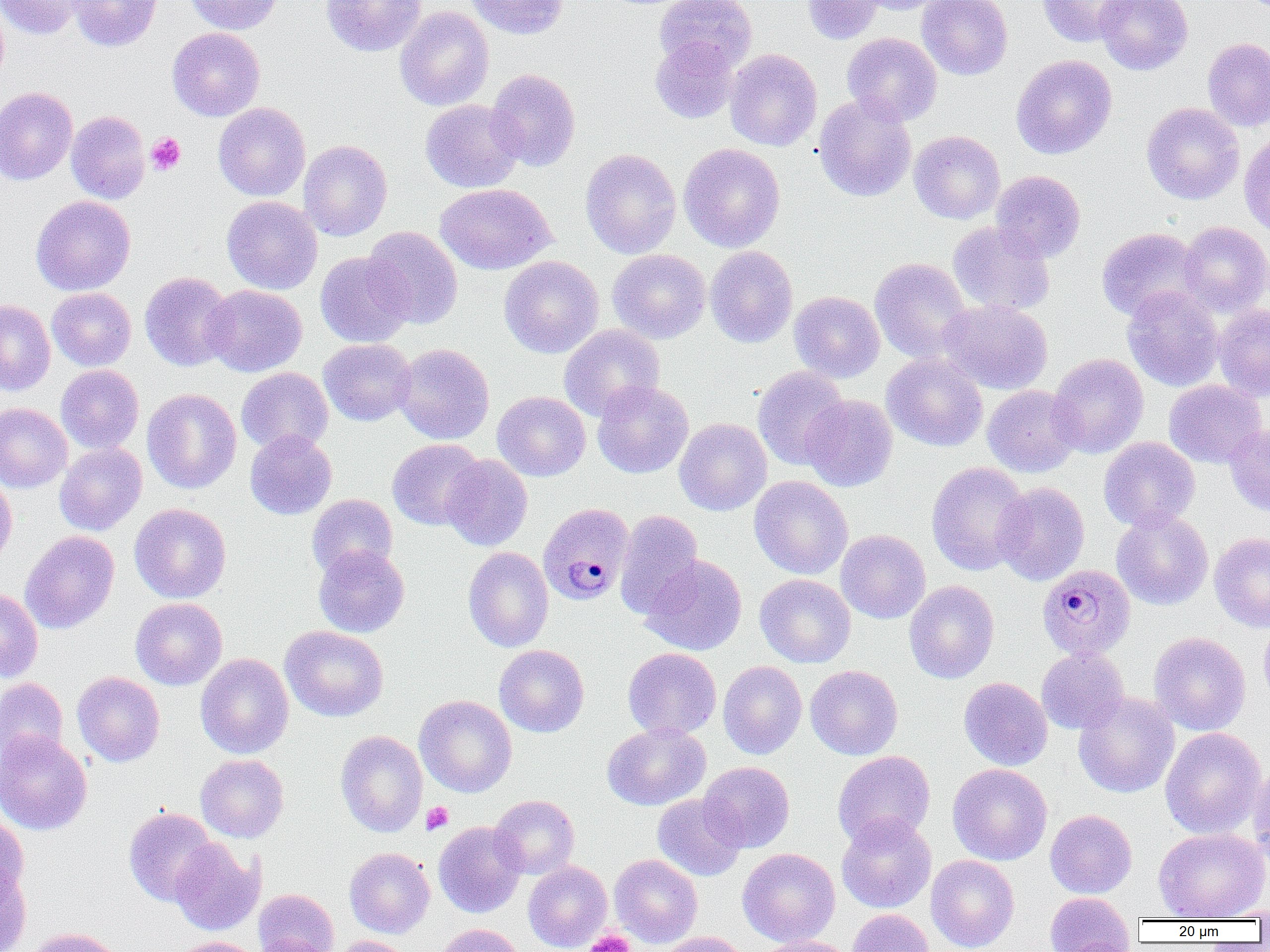

slide-level diagnosis = Plasmodium malariae
uninfected red blood cell locations = approximate bounding boxes as named x1/y1/x2/y2 corners in pixels: (x1=0, y1=0, x2=85, y2=39), (x1=66, y1=0, x2=162, y2=52), (x1=184, y1=0, x2=283, y2=34), (x1=321, y1=0, x2=426, y2=56), (x1=464, y1=0, x2=570, y2=39), (x1=655, y1=0, x2=757, y2=73), (x1=801, y1=0, x2=885, y2=44), (x1=857, y1=0, x2=950, y2=15), (x1=916, y1=0, x2=1013, y2=80), (x1=1037, y1=0, x2=1138, y2=47), (x1=1095, y1=0, x2=1193, y2=75), (x1=394, y1=6, x2=494, y2=111), (x1=167, y1=27, x2=265, y2=121), (x1=842, y1=33, x2=942, y2=126), (x1=650, y1=37, x2=740, y2=124), (x1=1202, y1=37, x2=1270, y2=132), (x1=725, y1=49, x2=822, y2=151), (x1=1011, y1=54, x2=1117, y2=159), (x1=486, y1=68, x2=581, y2=171), (x1=0, y1=87, x2=78, y2=185), (x1=813, y1=94, x2=917, y2=202), (x1=420, y1=99, x2=525, y2=192), (x1=213, y1=102, x2=311, y2=201), (x1=1141, y1=102, x2=1245, y2=205), (x1=66, y1=111, x2=151, y2=204), (x1=909, y1=130, x2=1005, y2=224), (x1=1239, y1=134, x2=1270, y2=238), (x1=299, y1=140, x2=392, y2=241), (x1=678, y1=143, x2=785, y2=252), (x1=580, y1=148, x2=682, y2=259), (x1=990, y1=170, x2=1086, y2=262), (x1=435, y1=183, x2=555, y2=274), (x1=30, y1=195, x2=136, y2=295), (x1=222, y1=196, x2=323, y2=294), (x1=948, y1=221, x2=1055, y2=316), (x1=1178, y1=221, x2=1270, y2=316), (x1=363, y1=226, x2=463, y2=329), (x1=1097, y1=227, x2=1204, y2=323), (x1=704, y1=246, x2=798, y2=348), (x1=608, y1=249, x2=710, y2=344), (x1=315, y1=251, x2=413, y2=347), (x1=499, y1=256, x2=603, y2=358), (x1=870, y1=258, x2=973, y2=363), (x1=139, y1=271, x2=236, y2=371), (x1=202, y1=285, x2=307, y2=377), (x1=1122, y1=285, x2=1223, y2=391), (x1=47, y1=287, x2=136, y2=371), (x1=789, y1=291, x2=884, y2=383), (x1=0, y1=300, x2=55, y2=396), (x1=939, y1=300, x2=1052, y2=394), (x1=1214, y1=303, x2=1270, y2=402), (x1=558, y1=325, x2=665, y2=421), (x1=318, y1=338, x2=416, y2=426), (x1=393, y1=343, x2=495, y2=444), (x1=882, y1=353, x2=988, y2=452), (x1=1048, y1=353, x2=1149, y2=458), (x1=55, y1=365, x2=144, y2=454), (x1=752, y1=366, x2=850, y2=470), (x1=236, y1=368, x2=333, y2=454), (x1=1163, y1=379, x2=1267, y2=468), (x1=592, y1=381, x2=693, y2=478), (x1=982, y1=385, x2=1082, y2=477), (x1=142, y1=389, x2=241, y2=494), (x1=492, y1=391, x2=590, y2=481), (x1=801, y1=395, x2=898, y2=492), (x1=0, y1=403, x2=72, y2=492), (x1=674, y1=418, x2=772, y2=516), (x1=1224, y1=424, x2=1270, y2=517), (x1=245, y1=430, x2=337, y2=520), (x1=1099, y1=437, x2=1200, y2=532), (x1=387, y1=438, x2=486, y2=530), (x1=54, y1=443, x2=147, y2=535), (x1=440, y1=454, x2=533, y2=551), (x1=926, y1=462, x2=1032, y2=576), (x1=0, y1=472, x2=17, y2=568), (x1=749, y1=476, x2=853, y2=579), (x1=993, y1=482, x2=1090, y2=585), (x1=306, y1=493, x2=398, y2=579), (x1=130, y1=503, x2=231, y2=603), (x1=1111, y1=508, x2=1213, y2=611), (x1=614, y1=510, x2=704, y2=619), (x1=836, y1=529, x2=930, y2=624), (x1=20, y1=531, x2=119, y2=633), (x1=1209, y1=532, x2=1270, y2=632), (x1=313, y1=545, x2=410, y2=638), (x1=463, y1=547, x2=554, y2=652), (x1=641, y1=555, x2=747, y2=656), (x1=755, y1=574, x2=856, y2=668), (x1=904, y1=580, x2=999, y2=684), (x1=0, y1=588, x2=43, y2=683), (x1=130, y1=598, x2=227, y2=690), (x1=1258, y1=617, x2=1270, y2=711), (x1=280, y1=625, x2=389, y2=722), (x1=1148, y1=631, x2=1251, y2=735), (x1=494, y1=645, x2=590, y2=737), (x1=623, y1=647, x2=721, y2=740), (x1=1036, y1=648, x2=1129, y2=734), (x1=195, y1=653, x2=294, y2=758), (x1=719, y1=660, x2=807, y2=759), (x1=805, y1=665, x2=903, y2=760), (x1=72, y1=672, x2=165, y2=766), (x1=0, y1=677, x2=68, y2=769), (x1=959, y1=677, x2=1053, y2=770), (x1=1073, y1=691, x2=1179, y2=798), (x1=414, y1=695, x2=517, y2=797), (x1=602, y1=722, x2=711, y2=810), (x1=1160, y1=727, x2=1266, y2=838), (x1=335, y1=730, x2=427, y2=837), (x1=0, y1=731, x2=91, y2=835), (x1=832, y1=750, x2=936, y2=848), (x1=195, y1=754, x2=289, y2=843), (x1=698, y1=762, x2=795, y2=852), (x1=947, y1=763, x2=1052, y2=865), (x1=1249, y1=763, x2=1270, y2=866), (x1=490, y1=794, x2=579, y2=879), (x1=652, y1=794, x2=747, y2=881), (x1=123, y1=807, x2=219, y2=905), (x1=1045, y1=809, x2=1137, y2=898), (x1=836, y1=814, x2=936, y2=913), (x1=0, y1=815, x2=29, y2=901), (x1=433, y1=821, x2=526, y2=918), (x1=1154, y1=828, x2=1269, y2=920), (x1=169, y1=839, x2=264, y2=935), (x1=344, y1=847, x2=435, y2=938), (x1=737, y1=847, x2=840, y2=947), (x1=609, y1=854, x2=702, y2=947), (x1=926, y1=854, x2=1019, y2=952), (x1=523, y1=861, x2=611, y2=951), (x1=0, y1=863, x2=31, y2=952), (x1=253, y1=888, x2=339, y2=952), (x1=1044, y1=892, x2=1134, y2=951), (x1=1214, y1=905, x2=1270, y2=921), (x1=847, y1=909, x2=934, y2=952), (x1=435, y1=923, x2=526, y2=952), (x1=25, y1=927, x2=125, y2=952), (x1=657, y1=932, x2=750, y2=952), (x1=250, y1=934, x2=335, y2=951), (x1=174, y1=936, x2=262, y2=952), (x1=331, y1=936, x2=413, y2=952), (x1=750, y1=936, x2=855, y2=952), (x1=1057, y1=937, x2=1140, y2=952)
magnification = 1000x
field of view = single
platelet locations = approximate bounding boxes as named x1/y1/x2/y2 corners in pixels: (x1=146, y1=133, x2=186, y2=175), (x1=422, y1=801, x2=453, y2=835), (x1=585, y1=929, x2=635, y2=952)
image size = 1270×952 pixels
modality = optical microscopy
Plasmodium malariae-infected red blood cell locations = approximate bounding boxes as named x1/y1/x2/y2 corners in pixels: (x1=538, y1=502, x2=634, y2=605), (x1=1038, y1=564, x2=1136, y2=661)
preparation = thin blood film